Give the position of every Plasmodium parasite visible.
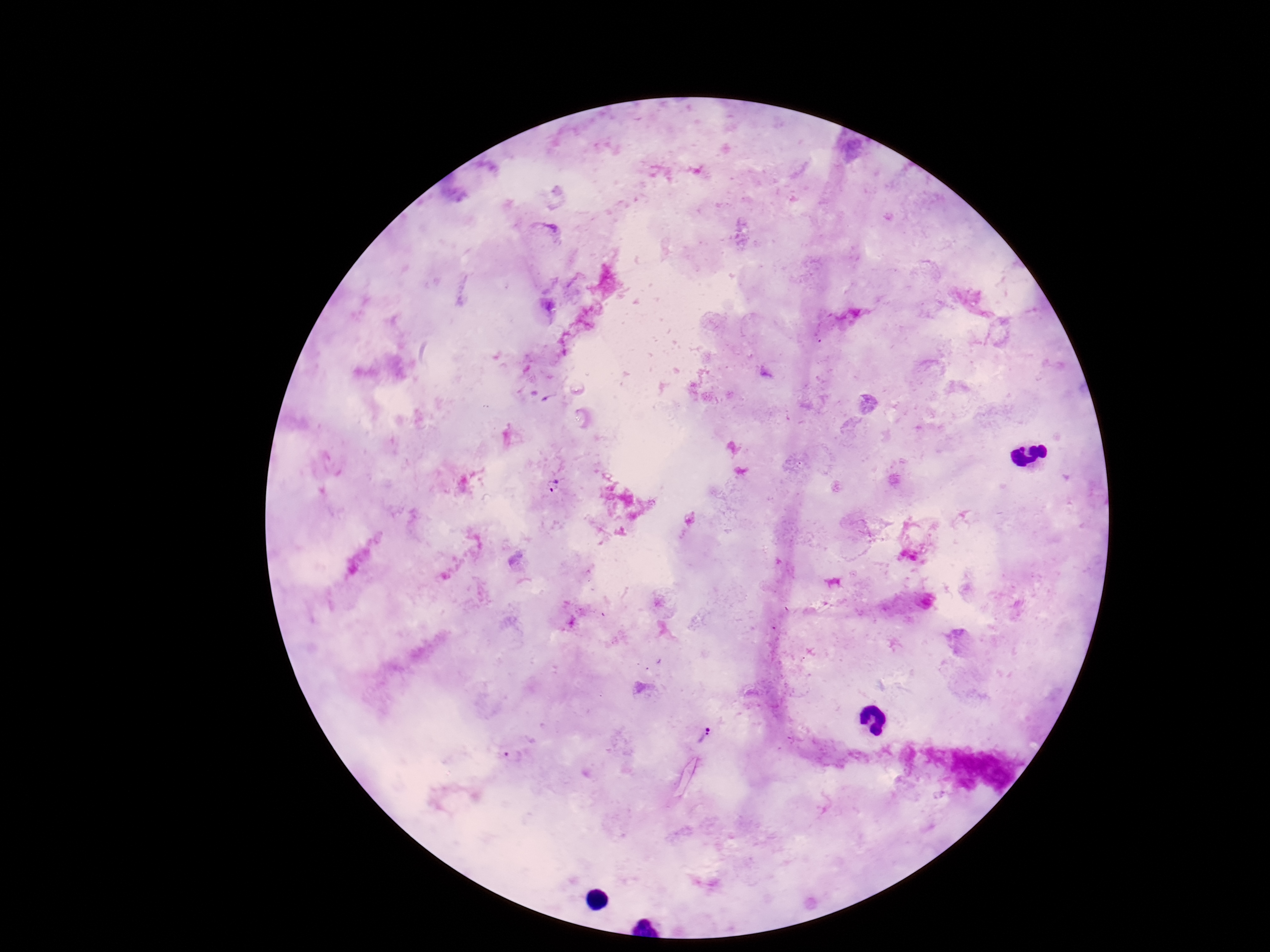

Approximate centers as {x, y} in pixels.
Plasmodium parasites: {551, 484}, {706, 739}, {511, 756}.

field of view = one from this slide
capture = smartphone camera through the microscope eyepiece
stain = Giemsa
image size = 1270×952 pixels
patient malaria status = infected
preparation = thick blood film
magnification = 100x